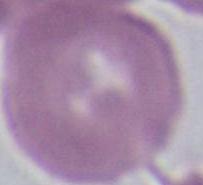

Summary:
  - Magnification: 1000x
  - Modality: micrograph
  - Identification: erythrocyte